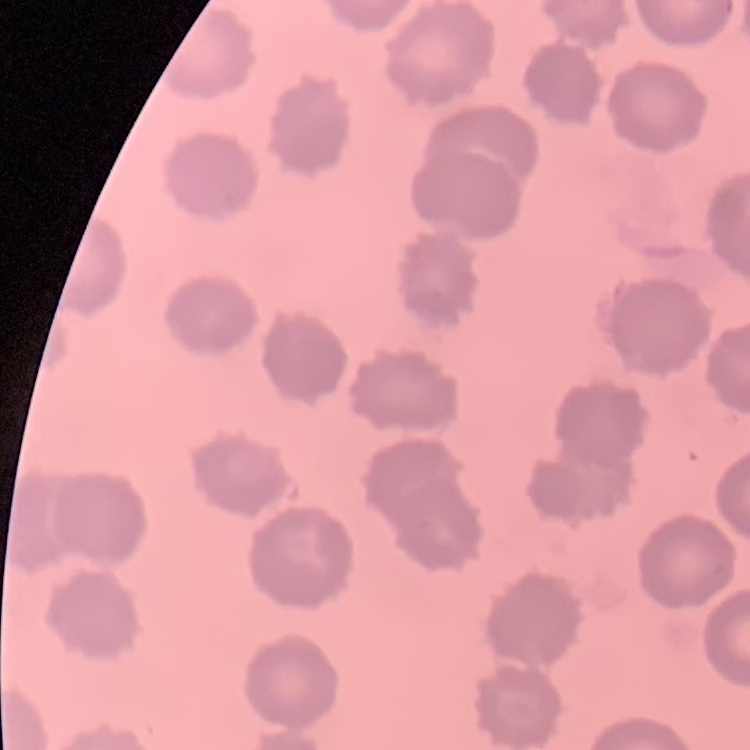
Summary:
  - Red blood cell morphology: no rouleaux formation
  - Image type: square crop of a larger photomicrograph
  - Stain: Field's or Giemsa
  - Preparation: thin blood smear